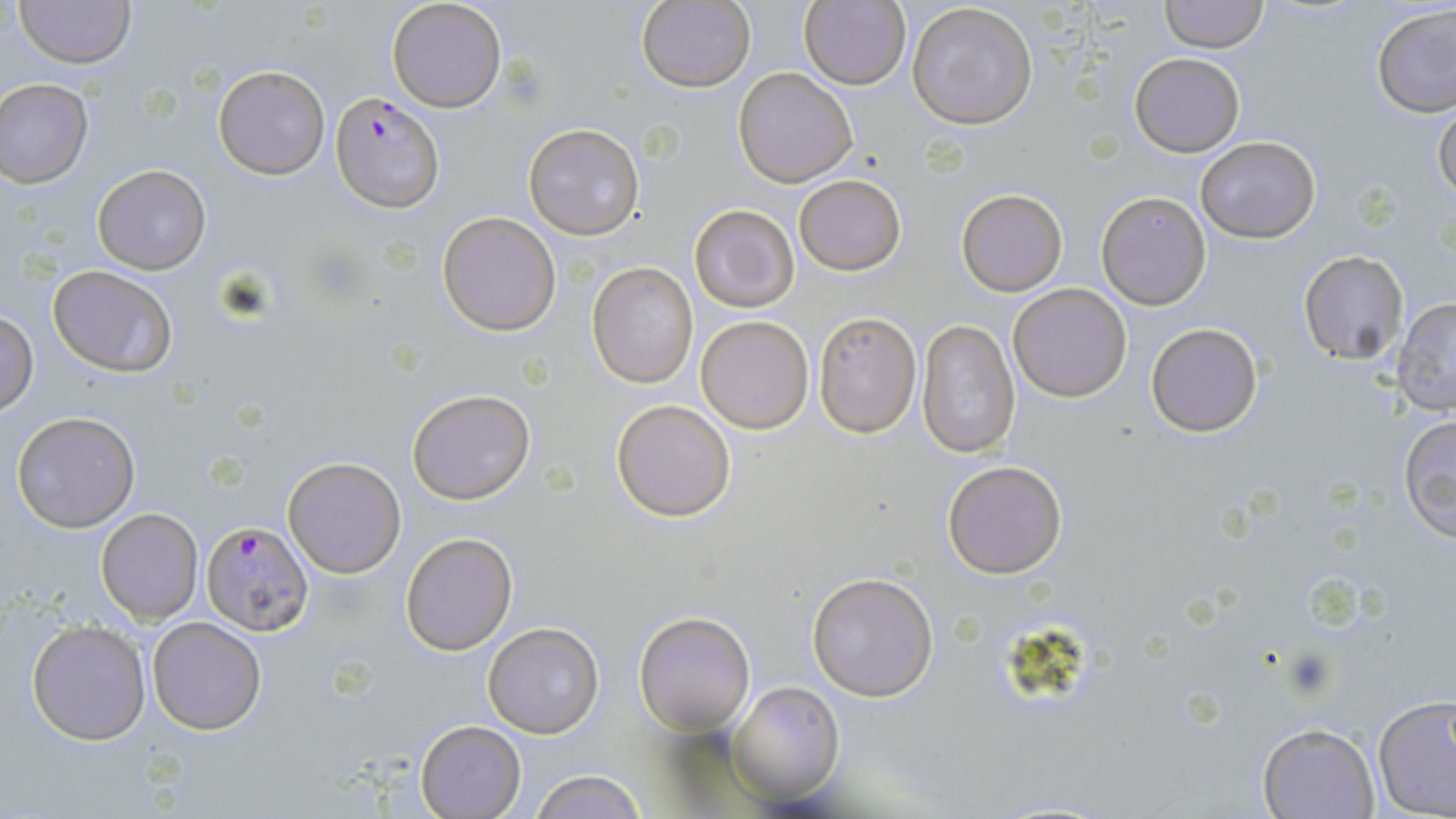
slide-level diagnosis = Plasmodium falciparum
magnification = 1000x
image size = 1456×819 pixels
Plasmodium falciparum-infected red blood cell locations = approximate bounding boxes as named x1/y1/x2/y2 corners in pixels: (x1=330, y1=91, x2=443, y2=210), (x1=200, y1=520, x2=315, y2=637)
field of view = one of a larger specimen
stain = May-Grünwald-Giemsa
modality = light microscopy
preparation = thin blood smear
uninfected red blood cell locations = approximate bounding boxes as named x1/y1/x2/y2 corners in pixels: (x1=15, y1=0, x2=134, y2=68), (x1=385, y1=0, x2=508, y2=114), (x1=1159, y1=0, x2=1268, y2=53), (x1=636, y1=1, x2=755, y2=92), (x1=798, y1=1, x2=911, y2=89), (x1=906, y1=4, x2=1039, y2=130), (x1=1372, y1=4, x2=1456, y2=117), (x1=1129, y1=52, x2=1245, y2=157), (x1=214, y1=65, x2=330, y2=180), (x1=733, y1=67, x2=859, y2=187), (x1=0, y1=78, x2=94, y2=187), (x1=1433, y1=99, x2=1455, y2=205), (x1=523, y1=123, x2=646, y2=240), (x1=1195, y1=136, x2=1321, y2=243), (x1=92, y1=164, x2=212, y2=275), (x1=794, y1=175, x2=906, y2=275), (x1=956, y1=188, x2=1069, y2=296), (x1=1096, y1=192, x2=1211, y2=309), (x1=689, y1=203, x2=800, y2=313), (x1=436, y1=211, x2=561, y2=336), (x1=1298, y1=250, x2=1411, y2=367), (x1=588, y1=261, x2=700, y2=389), (x1=49, y1=265, x2=177, y2=378), (x1=1007, y1=283, x2=1133, y2=402), (x1=1392, y1=298, x2=1456, y2=417), (x1=1, y1=308, x2=37, y2=415), (x1=811, y1=309, x2=923, y2=438), (x1=697, y1=314, x2=815, y2=435), (x1=916, y1=321, x2=1020, y2=459), (x1=1145, y1=321, x2=1265, y2=439), (x1=407, y1=388, x2=537, y2=504), (x1=611, y1=399, x2=737, y2=523), (x1=11, y1=410, x2=141, y2=533), (x1=1396, y1=412, x2=1456, y2=543), (x1=283, y1=457, x2=406, y2=578), (x1=942, y1=460, x2=1068, y2=579), (x1=96, y1=508, x2=203, y2=625), (x1=402, y1=532, x2=517, y2=655), (x1=806, y1=570, x2=939, y2=702), (x1=635, y1=609, x2=754, y2=735), (x1=147, y1=617, x2=268, y2=736), (x1=27, y1=620, x2=152, y2=746), (x1=482, y1=621, x2=604, y2=738), (x1=730, y1=682, x2=844, y2=805), (x1=1371, y1=690, x2=1456, y2=819), (x1=415, y1=720, x2=526, y2=818), (x1=1255, y1=720, x2=1380, y2=817), (x1=529, y1=770, x2=649, y2=818)